Identify the parasite.
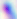
This is Toxoplasma gondii.

Summary:
  - Modality: photomicrograph
  - Magnification: 400x